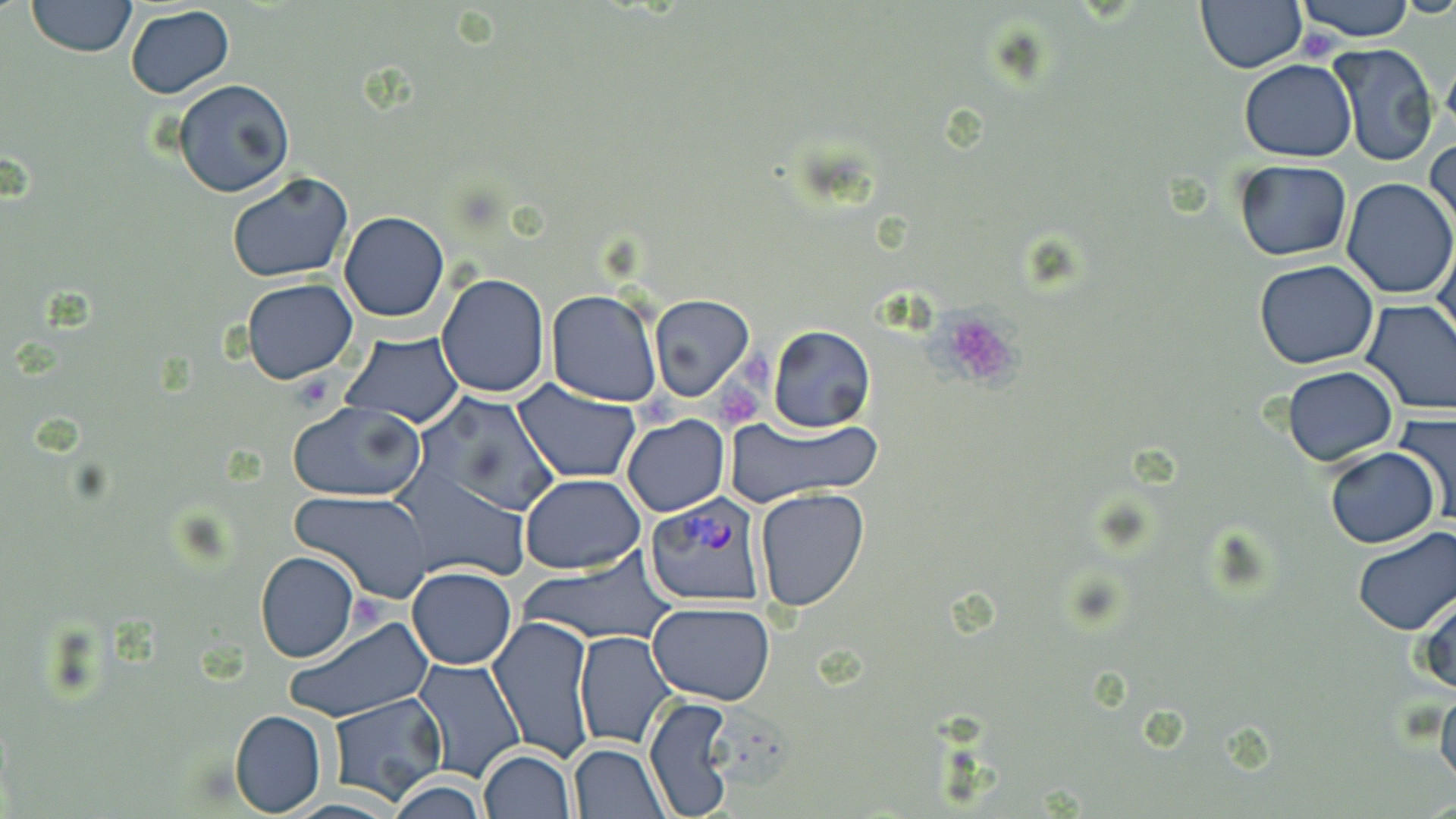
slide-level diagnosis = Plasmodium vivax
field of view = single
preparation = thin blood film
modality = optical microscopy
uninfected red blood cell locations = approximate bounding boxes as [x1, y1, x2, y2] in pixels: [26, 0, 137, 57], [1293, 0, 1420, 42], [1196, 1, 1306, 72], [124, 4, 234, 99], [1327, 41, 1439, 168], [1238, 59, 1358, 162], [174, 79, 295, 198], [1427, 135, 1455, 243], [1233, 159, 1352, 261], [227, 170, 356, 281], [1340, 179, 1455, 298], [339, 211, 450, 322], [1434, 235, 1456, 350], [1254, 260, 1380, 368], [436, 273, 550, 398], [241, 278, 358, 384], [546, 291, 663, 406], [648, 295, 754, 402], [1359, 301, 1456, 417], [768, 325, 875, 433], [340, 330, 465, 428], [1282, 366, 1396, 465], [513, 380, 640, 483], [414, 393, 561, 518], [287, 402, 427, 502], [1393, 412, 1456, 525], [622, 414, 729, 517], [726, 414, 876, 505], [1323, 446, 1439, 547], [396, 471, 533, 585], [520, 471, 645, 574], [754, 487, 868, 610], [293, 489, 434, 603], [1351, 528, 1456, 636], [255, 550, 359, 663], [517, 556, 676, 643], [406, 566, 516, 671], [1415, 587, 1456, 697], [648, 601, 776, 706], [487, 614, 597, 762], [281, 616, 432, 725], [573, 631, 675, 747], [411, 659, 526, 783], [1437, 680, 1456, 794], [329, 693, 448, 806], [644, 695, 734, 819], [229, 710, 326, 817], [568, 744, 670, 819], [478, 749, 575, 819], [384, 776, 490, 818]
image size = 1456×819 pixels
Plasmodium vivax-infected red blood cell locations = approximate bounding boxes as [x1, y1, x2, y2] in pixels: [644, 495, 769, 605]
platelet locations = approximate bounding boxes as [x1, y1, x2, y2] in pixels: [938, 312, 1023, 388], [736, 348, 773, 384], [695, 377, 764, 432], [633, 388, 685, 432]
magnification = 1000x
stain = May-Grünwald-Giemsa